Outline each blood parasite and name the species.
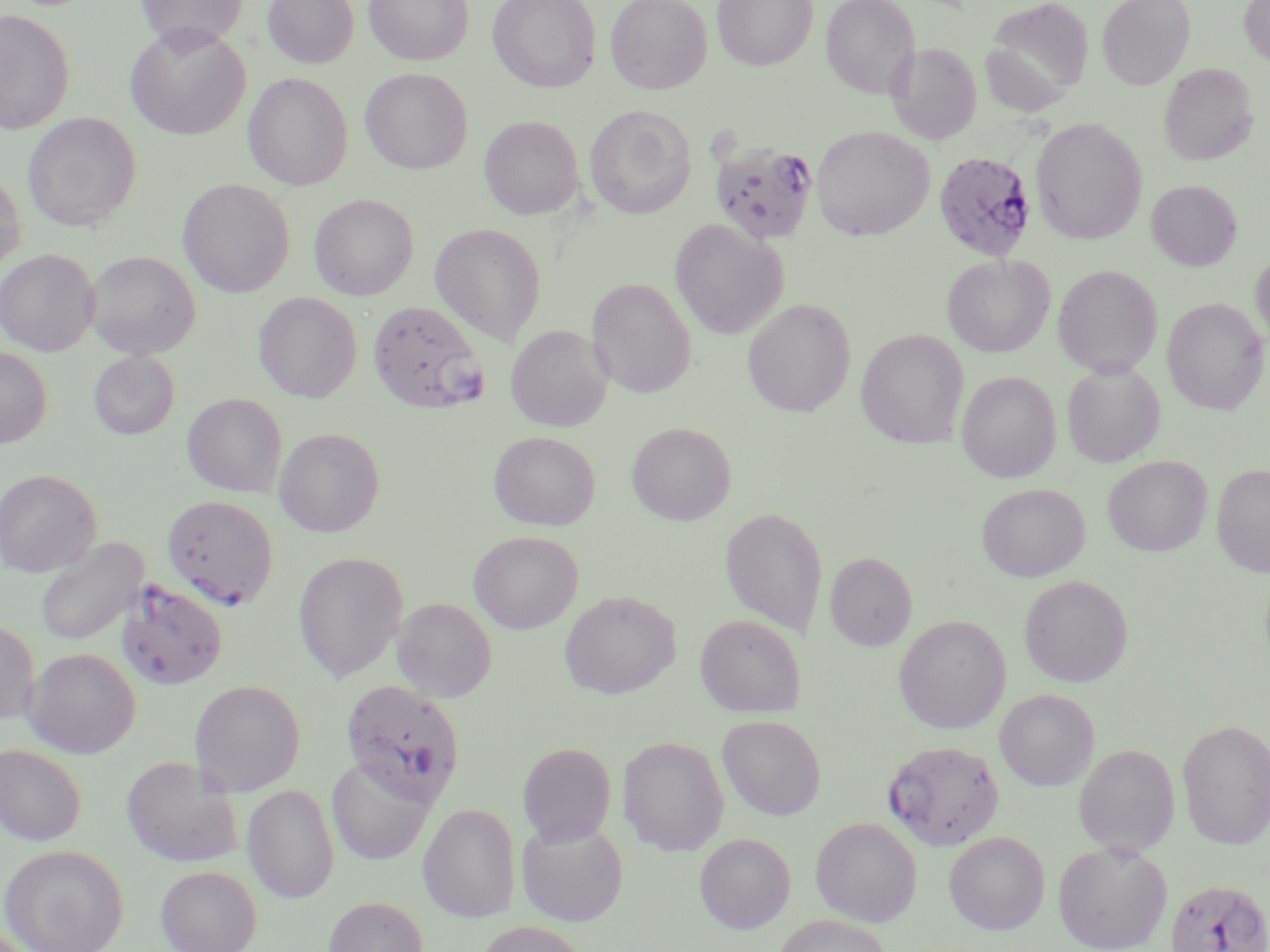
Approximate bounding boxes as [x1, y1, x2, y2] in pixels.
Plasmodium falciparum-infected red blood cells: [709, 138, 819, 245], [933, 151, 1037, 262], [367, 299, 487, 414], [162, 494, 279, 609], [116, 579, 229, 691], [341, 679, 465, 805], [883, 739, 1005, 851], [1164, 878, 1270, 952].
No Plasmodium ovale, Plasmodium malariae, Plasmodium vivax, Babesia divergens, or Trypanosoma brucei observed.

Uninfected red blood cell locations: [135, 0, 249, 51], [263, 0, 358, 68], [364, 0, 474, 66], [487, 0, 601, 92], [605, 0, 712, 94], [712, 0, 818, 71], [821, 0, 920, 99], [1096, 0, 1195, 90], [1239, 0, 1270, 68], [983, 1, 1093, 107], [0, 9, 75, 134], [125, 26, 250, 139], [887, 42, 982, 145], [1159, 63, 1257, 165], [360, 68, 473, 174], [243, 72, 353, 190], [584, 104, 696, 219], [22, 112, 142, 232], [479, 115, 585, 220], [1030, 117, 1147, 245], [811, 125, 933, 240], [0, 168, 26, 273], [178, 179, 295, 297], [1146, 180, 1242, 270], [309, 194, 418, 300], [670, 219, 788, 340], [430, 223, 547, 346], [1250, 248, 1270, 351], [0, 249, 100, 356], [84, 250, 201, 359], [942, 254, 1055, 357], [1052, 265, 1163, 376], [587, 278, 696, 398], [253, 292, 362, 403], [742, 298, 856, 417], [1162, 298, 1269, 415], [506, 325, 613, 431], [856, 328, 969, 448], [0, 347, 52, 447], [88, 350, 180, 440], [1062, 361, 1165, 467], [957, 371, 1061, 483], [182, 393, 287, 497], [627, 422, 736, 525], [273, 427, 385, 537], [488, 431, 601, 530], [1103, 455, 1212, 556], [1211, 463, 1270, 576], [0, 468, 102, 577], [976, 483, 1089, 581], [720, 507, 829, 638], [468, 530, 583, 633], [34, 537, 148, 647], [293, 551, 409, 683], [825, 551, 917, 650], [1019, 575, 1133, 687], [559, 589, 681, 698], [392, 597, 497, 703], [695, 614, 806, 717], [893, 615, 1011, 733], [0, 619, 39, 725], [24, 647, 141, 757], [189, 679, 306, 796], [994, 689, 1099, 790], [717, 715, 826, 820], [1177, 719, 1270, 849], [618, 735, 730, 856], [517, 742, 617, 845], [1073, 743, 1180, 856], [0, 744, 87, 845], [121, 755, 242, 868], [326, 756, 436, 865], [242, 783, 340, 903], [418, 803, 521, 922], [811, 816, 922, 926], [516, 818, 628, 926], [943, 831, 1050, 934], [694, 832, 795, 933], [1052, 840, 1173, 952], [0, 844, 129, 952], [156, 865, 261, 952], [323, 895, 429, 952], [773, 914, 893, 952], [475, 920, 591, 952]. Slide-level diagnosis: Plasmodium falciparum. Captured at 1000x magnification. Optical microscopy. Single field of view. May-Grünwald-Giemsa-stained preparation. Thin blood smear. Image is 1270×952 pixels.